Report the malaria status of this cell.
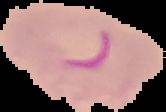

Parasitized.

image_size: 166×112 pixels
image_type: segmented cell region with the area outside set to black
preparation: thin blood smear